Name the parasite shown.
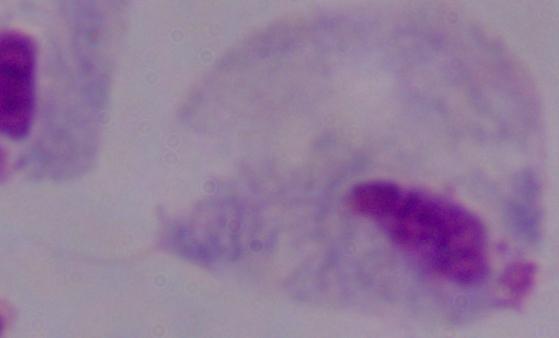

This is a trichomonad.

Summary:
  - Magnification: 1000x
  - Modality: micrograph